Describe the morphology of the erythrocytes.
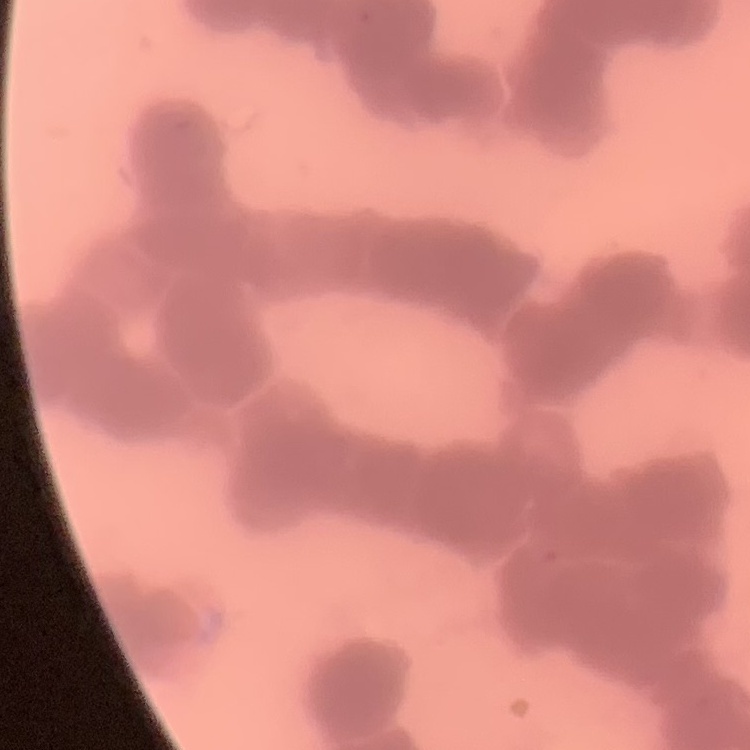

They show rouleaux formation.

Summary:
  - Image type: one tile cut from a larger photomicrograph
  - Stain: Field's or Giemsa
  - Preparation: thin blood film